Assess this cell for malaria.
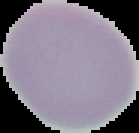
It is uninfected.

Cell region segmented out of the field of view; the surrounding area is masked to black. Image is 139×133 pixels. From a thin blood film.